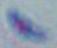
Summary:
  - Modality: micrograph
  - Magnification: 1000x
  - Identification: Toxoplasma gondii